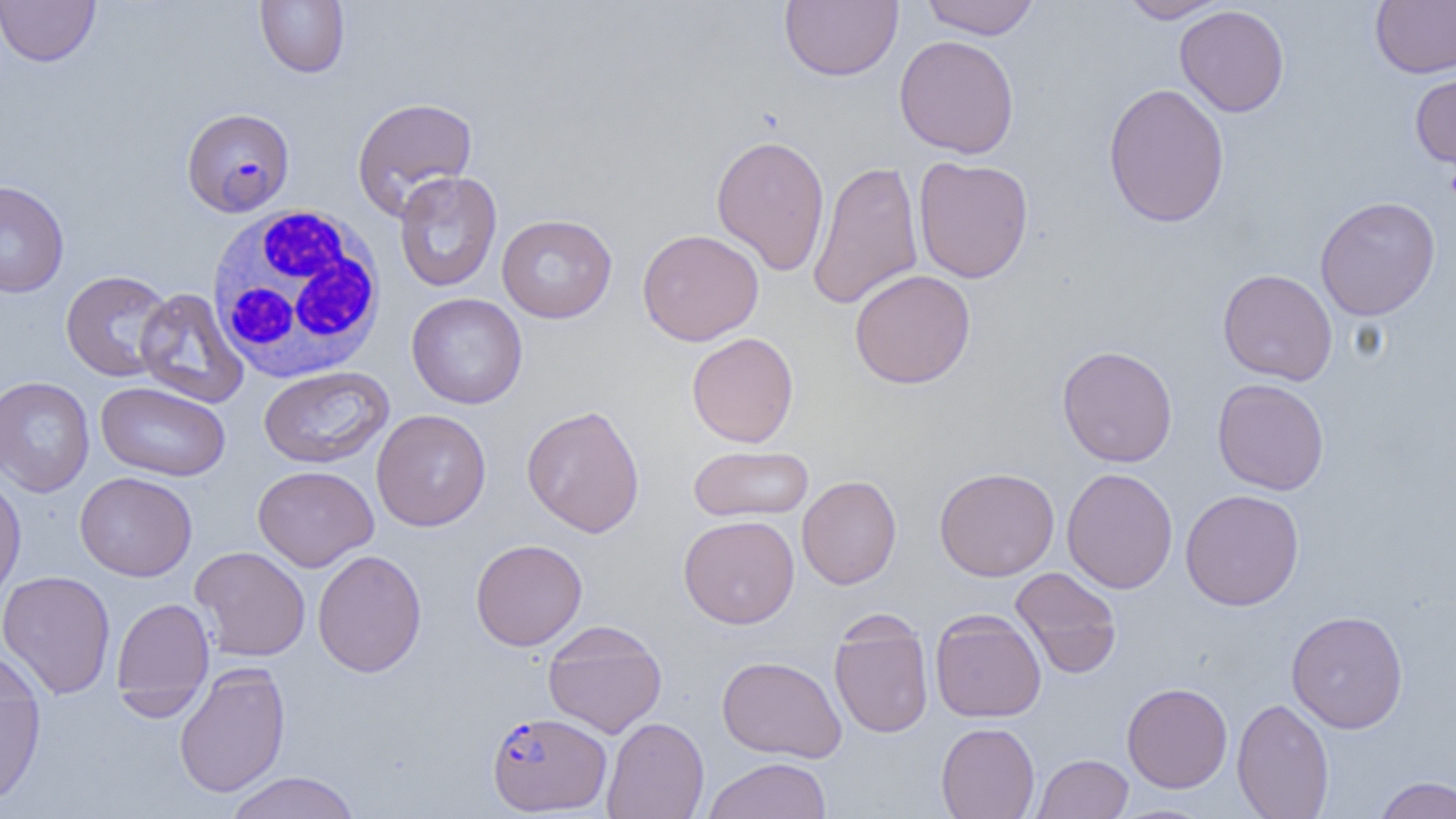
Summary:
  - Coordinate format: approximate bounding boxes as [x1, y1, x2, y2] in pixels
  - Uninfected red blood cell locations: [0, 0, 100, 67], [255, 0, 349, 78], [780, 0, 903, 81], [921, 0, 1039, 39], [1118, 0, 1228, 23], [1370, 0, 1456, 78], [1174, 4, 1290, 117], [894, 34, 1020, 159], [1409, 69, 1456, 170], [1102, 82, 1230, 229], [351, 96, 478, 219], [711, 134, 830, 276], [913, 156, 1034, 283], [807, 159, 924, 311], [393, 171, 502, 292], [0, 180, 70, 297], [1315, 196, 1441, 321], [496, 214, 618, 323], [637, 228, 764, 345], [1217, 268, 1338, 386], [61, 269, 174, 383], [849, 269, 976, 389], [134, 287, 249, 408], [407, 293, 528, 409], [686, 332, 799, 448], [1057, 345, 1178, 468], [258, 365, 394, 468], [0, 376, 95, 497], [1212, 378, 1330, 495], [95, 381, 230, 481], [522, 405, 645, 537], [371, 409, 491, 532], [688, 444, 814, 522], [253, 465, 378, 572], [934, 467, 1060, 581], [1062, 468, 1178, 593], [74, 471, 197, 581], [0, 473, 26, 605], [797, 475, 902, 590], [1180, 489, 1305, 611], [678, 515, 799, 628], [470, 539, 588, 651], [190, 546, 311, 661], [190, 549, 302, 798], [312, 549, 427, 677], [1010, 567, 1123, 679], [0, 570, 115, 699], [111, 596, 214, 716], [930, 609, 1046, 723], [1286, 610, 1408, 733], [828, 614, 935, 739], [542, 620, 667, 738], [717, 655, 846, 762], [0, 657, 46, 808], [173, 663, 291, 797], [1122, 682, 1232, 792], [1232, 698, 1335, 819], [602, 716, 709, 819], [935, 722, 1040, 819], [1032, 753, 1133, 818], [701, 757, 832, 818], [224, 771, 362, 819], [1372, 776, 1456, 818]
  - Plasmodium falciparum-infected red blood cell locations: [182, 108, 295, 217], [487, 711, 611, 815]
  - White blood cell locations: [205, 205, 388, 383]
  - Slide-level diagnosis: Plasmodium falciparum
  - Preparation: thin blood film
  - Image size: 1456×819 pixels
  - Magnification: 1000x
  - Modality: optical microscopy
  - Field of view: one of a larger specimen